Locate and identify every blood parasite.
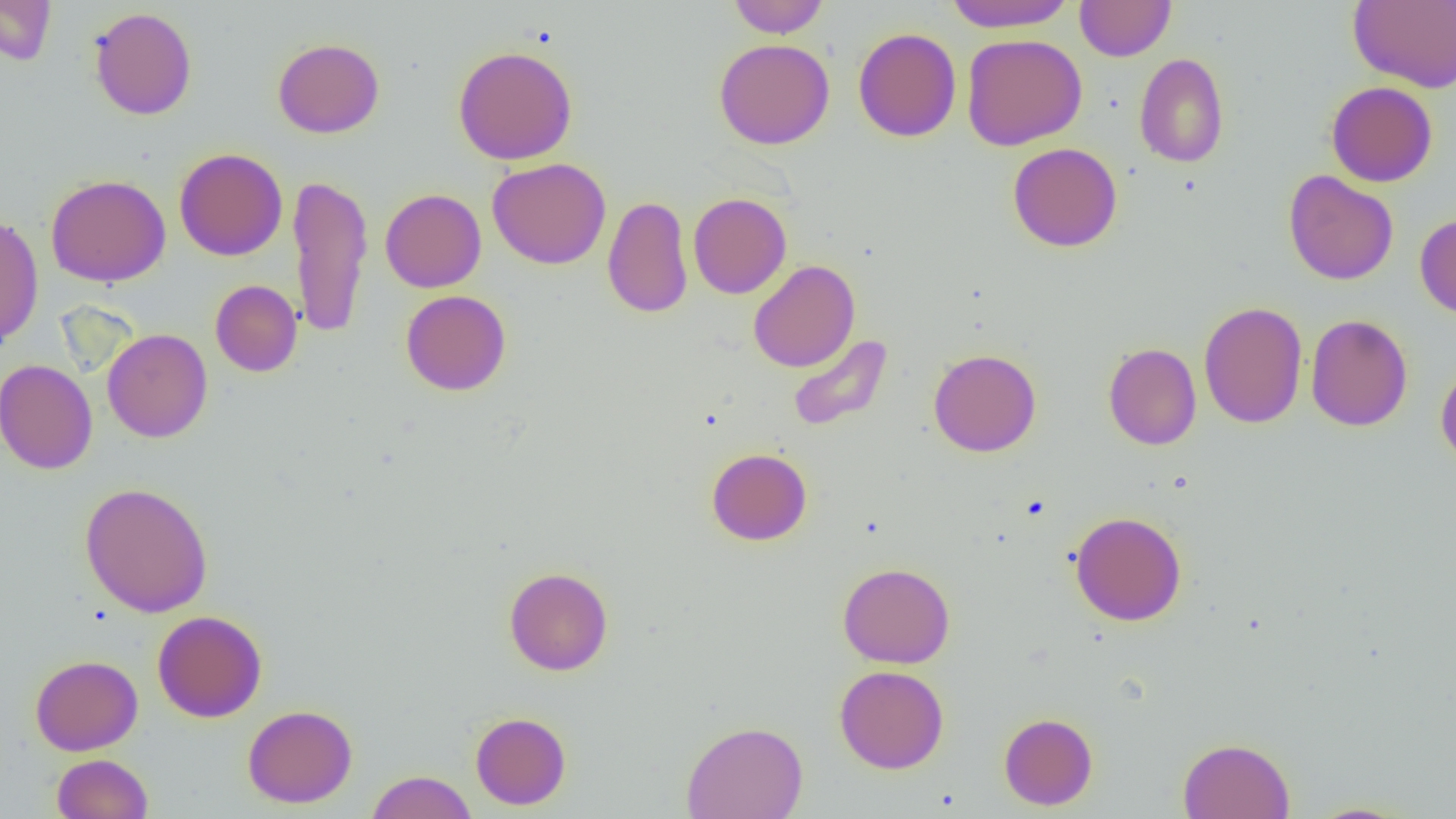
No blood parasites seen.

Approximate bounding boxes as [x1, y1, x2, y2] in pixels. Uninfected red blood cell locations: [0, 0, 56, 65], [727, 0, 830, 38], [944, 0, 1075, 32], [1075, 0, 1176, 61], [1348, 1, 1456, 92], [89, 7, 197, 120], [853, 28, 961, 142], [961, 33, 1087, 151], [272, 37, 384, 138], [714, 38, 835, 150], [453, 45, 578, 164], [1134, 52, 1229, 168], [1326, 81, 1438, 187], [1007, 143, 1122, 252], [175, 147, 288, 261], [487, 157, 611, 270], [1283, 170, 1398, 285], [288, 173, 373, 339], [46, 174, 170, 286], [380, 188, 486, 292], [688, 193, 792, 299], [602, 195, 693, 318], [1415, 213, 1456, 320], [0, 214, 44, 346], [748, 260, 860, 372], [210, 280, 302, 377], [401, 290, 511, 395], [1198, 300, 1307, 429], [1306, 314, 1413, 431], [102, 328, 213, 443], [786, 333, 893, 432], [1103, 342, 1202, 451], [928, 348, 1041, 457], [0, 359, 97, 474], [1435, 362, 1456, 470], [706, 447, 812, 545], [80, 482, 214, 617], [1069, 511, 1188, 626], [837, 562, 955, 668], [503, 566, 613, 676], [152, 610, 267, 722], [30, 655, 143, 755], [834, 664, 949, 774], [243, 704, 358, 808], [470, 711, 571, 810], [999, 712, 1098, 810], [681, 720, 808, 819], [1178, 737, 1294, 819], [52, 753, 153, 818], [365, 770, 477, 819], [1305, 801, 1417, 818]. Slide-level diagnosis: no evidence of blood parasites. Captured at 1000x magnification. Image is 1456×819 pixels. Thin blood film. Single field of view. Optical microscopy.